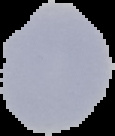

Image is 115×136 pixels. Result: negative for Plasmodium parasites. Cell region segmented out of the field of view; the surrounding area is masked to black. From a thin blood film.